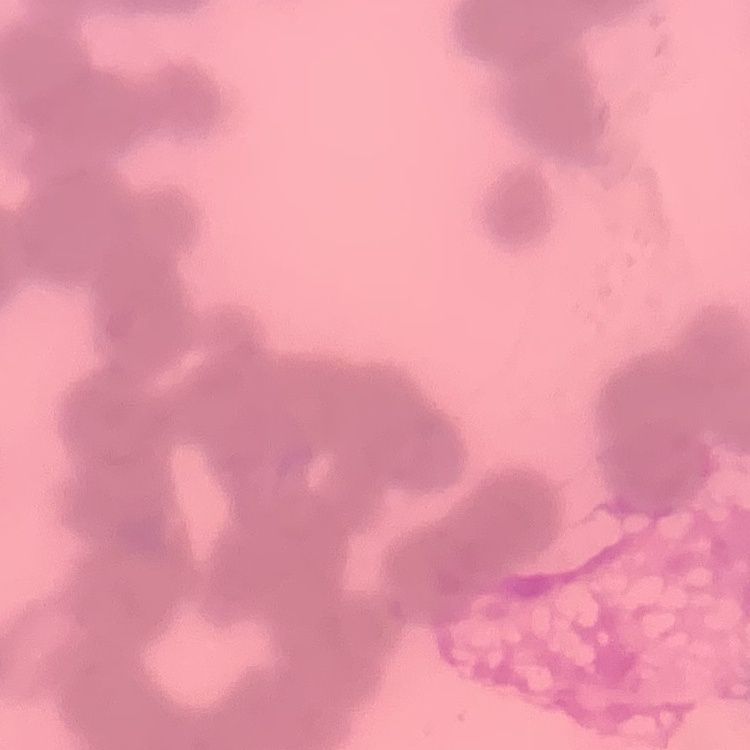
erythrocyte morphology = rouleaux formation
stain = Field's or Giemsa
image type = one tile cut from a larger photomicrograph
preparation = thin peripheral smear